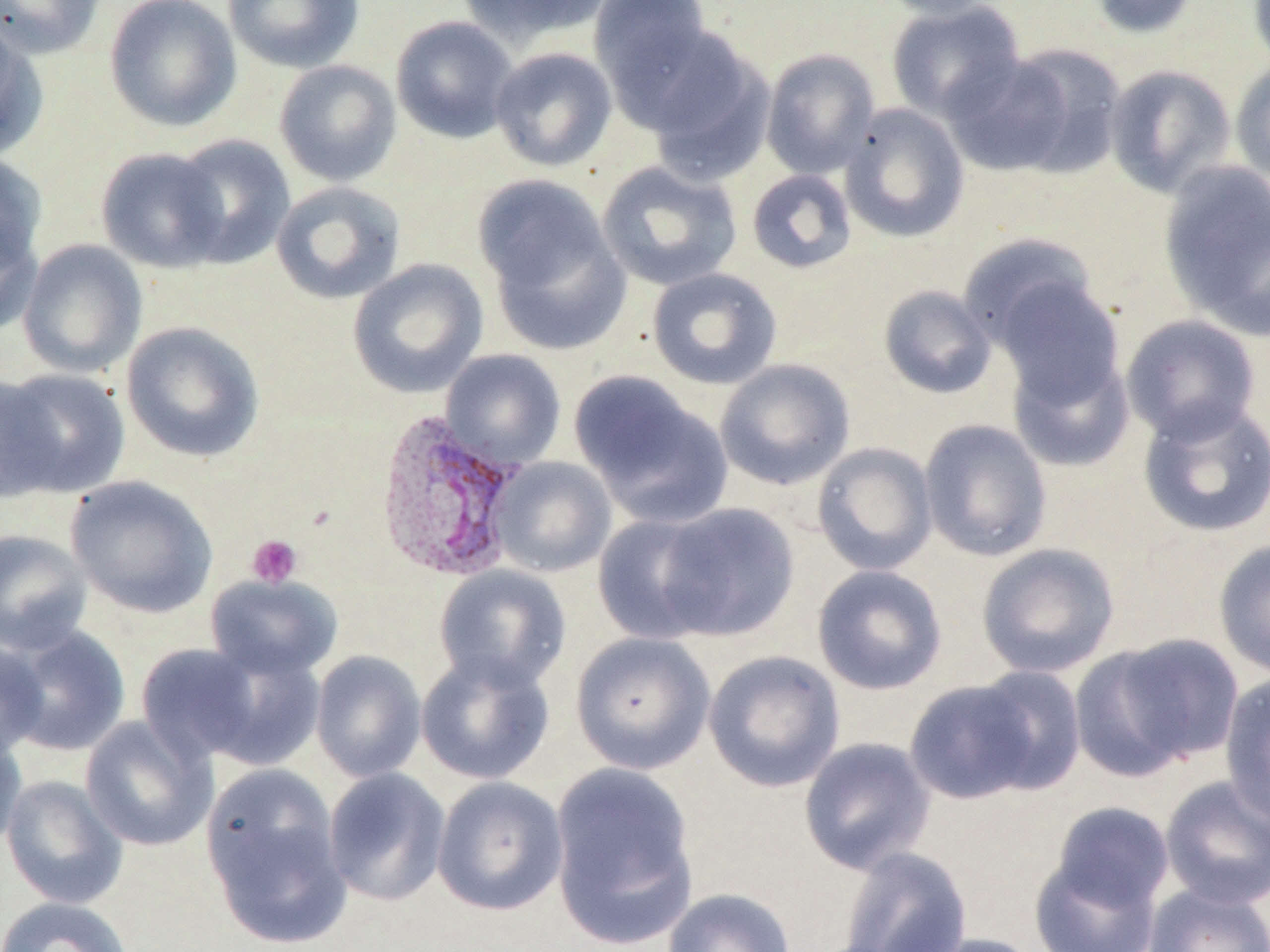
Summary:
  - Coordinate format: approximate bounding boxes as (x1,y1)-(x2,y2) corner pairs in pixels
  - Platelet locations: (247,535)-(302,587)
  - Plasmodium vivax-infected red blood cell locations: (373,409)-(525,581)
  - Uninfected red blood cell locations: (0,0)-(106,59), (104,0)-(242,133), (223,0)-(365,73), (458,0)-(611,48), (873,0)-(1003,21), (1087,0)-(1200,39), (1248,0)-(1270,72), (589,1)-(716,106), (885,1)-(1025,123), (390,16)-(519,144), (0,17)-(46,160), (636,28)-(776,182), (489,46)-(617,171), (761,48)-(880,179), (942,50)-(1099,178), (273,59)-(402,187), (1229,60)-(1270,185), (1104,64)-(1236,198), (839,103)-(970,243), (169,134)-(296,269), (96,146)-(229,272), (0,152)-(47,276), (596,161)-(743,292), (1159,161)-(1270,335), (746,168)-(857,274), (477,179)-(631,354), (271,181)-(406,305), (0,212)-(42,337), (958,234)-(1103,357), (18,239)-(148,378), (346,259)-(489,398), (646,267)-(783,390), (989,273)-(1127,404), (878,285)-(997,399), (1120,314)-(1263,444), (120,321)-(266,463), (1006,348)-(1135,473), (440,349)-(567,470), (714,358)-(856,490), (0,367)-(130,499), (571,373)-(732,528), (1137,399)-(1270,539), (918,419)-(1052,562), (812,442)-(938,576), (490,456)-(616,577), (65,475)-(218,618), (653,502)-(800,642), (591,514)-(721,644), (0,528)-(93,655), (1213,539)-(1270,679), (976,542)-(1121,679), (434,564)-(571,693), (812,564)-(947,695), (206,574)-(342,680), (5,625)-(131,757), (570,631)-(716,774), (1082,631)-(1244,773), (0,636)-(48,760), (135,643)-(265,765), (199,646)-(327,771), (703,649)-(846,793), (310,650)-(427,782), (415,652)-(554,786), (970,665)-(1087,795), (1220,671)-(1270,825), (904,678)-(1042,805), (80,716)-(217,852), (0,729)-(28,853), (798,736)-(936,875), (549,763)-(698,946), (201,767)-(351,946), (323,767)-(451,906), (1,775)-(128,909), (432,775)-(569,916), (1158,775)-(1270,910), (1049,802)-(1175,914), (838,845)-(973,952), (1029,854)-(1162,952), (1143,883)-(1270,952), (662,887)-(797,951), (0,896)-(134,952), (912,933)-(1048,952)
  - Slide-level diagnosis: Plasmodium vivax
  - Magnification: 1000x
  - Preparation: thin blood smear
  - Image size: 1270×952 pixels
  - Modality: light microscopy
  - Field of view: one of a larger specimen